State which cell type is depicted.
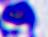

This is a leukocyte.

400x magnification. Photomicrograph.